Name the cell type shown.
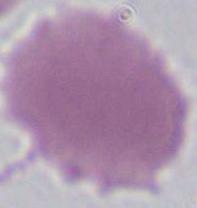

This is an erythrocyte.

Summary:
  - Magnification: 1000x
  - Modality: photomicrograph